Classify this cell by malaria status.
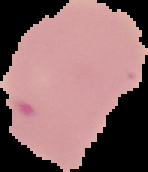
It is parasitized.

image type = cell region segmented out of the field of view; surrounding area masked to black
image size = 148×172 pixels
preparation = thin blood smear